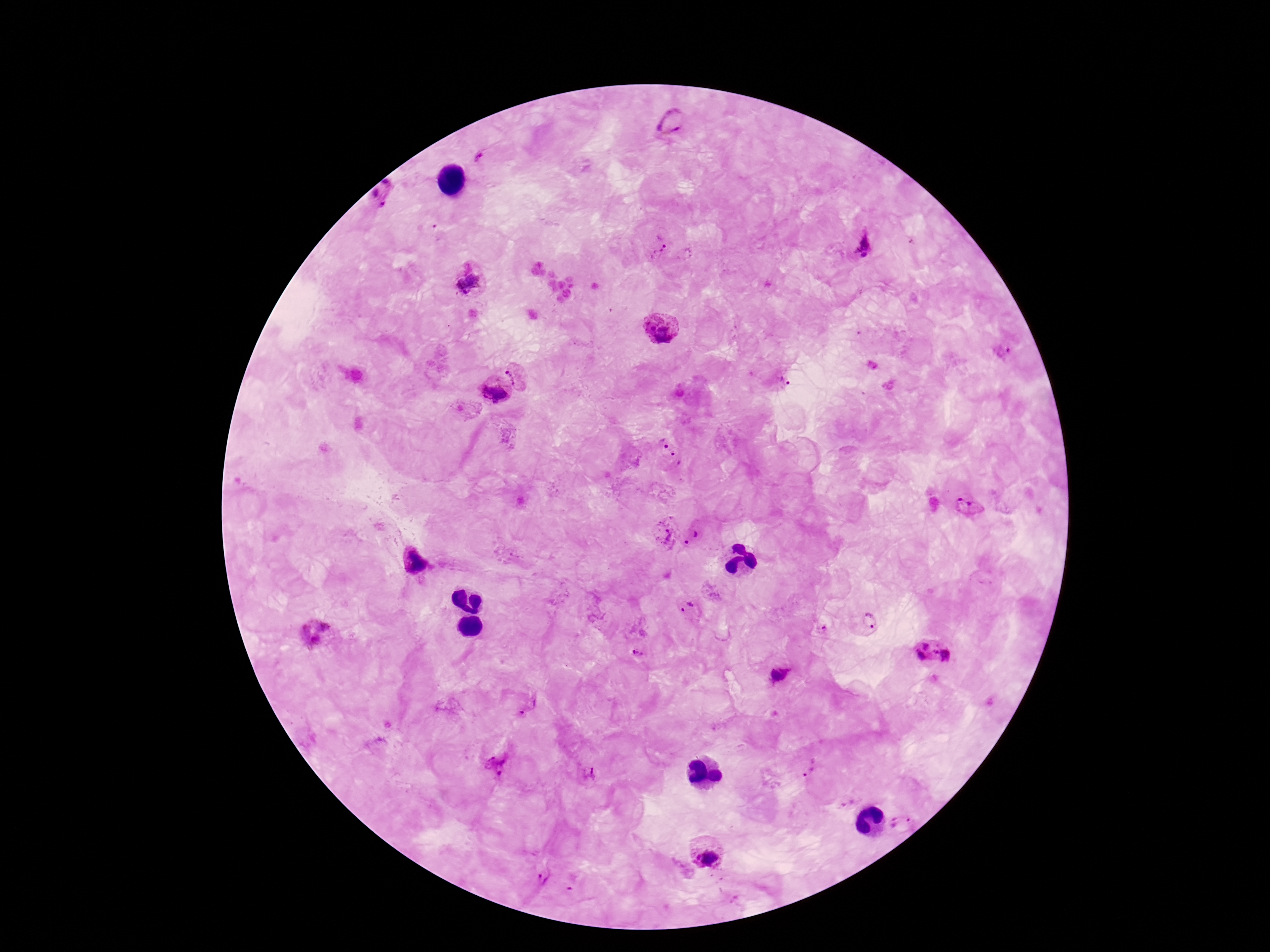

Approximate object centers, in pixels from the top-left corner. Plasmodium parasite locations: (x=671, y=123), (x=482, y=157), (x=384, y=194), (x=862, y=244), (x=656, y=245), (x=685, y=256), (x=468, y=284), (x=659, y=329), (x=1002, y=352), (x=519, y=372), (x=779, y=379), (x=491, y=394), (x=669, y=455), (x=970, y=507), (x=663, y=531), (x=692, y=537), (x=689, y=608), (x=869, y=621), (x=824, y=630), (x=314, y=634), (x=638, y=653), (x=934, y=654), (x=780, y=675), (x=529, y=706), (x=495, y=765), (x=810, y=766), (x=589, y=774), (x=846, y=802), (x=902, y=826), (x=705, y=849), (x=543, y=878). Giemsa-stained preparation. Smartphone photograph taken through the microscope eyepiece. Image is 1270×952 pixels. Patient malaria status: infected. Thick peripheral-blood smear. One field from this slide. 100x magnification.